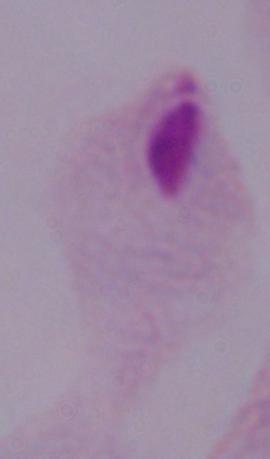

modality = micrograph
magnification = 1000x
identification = trichomonad